Outline each blood parasite and name the species.
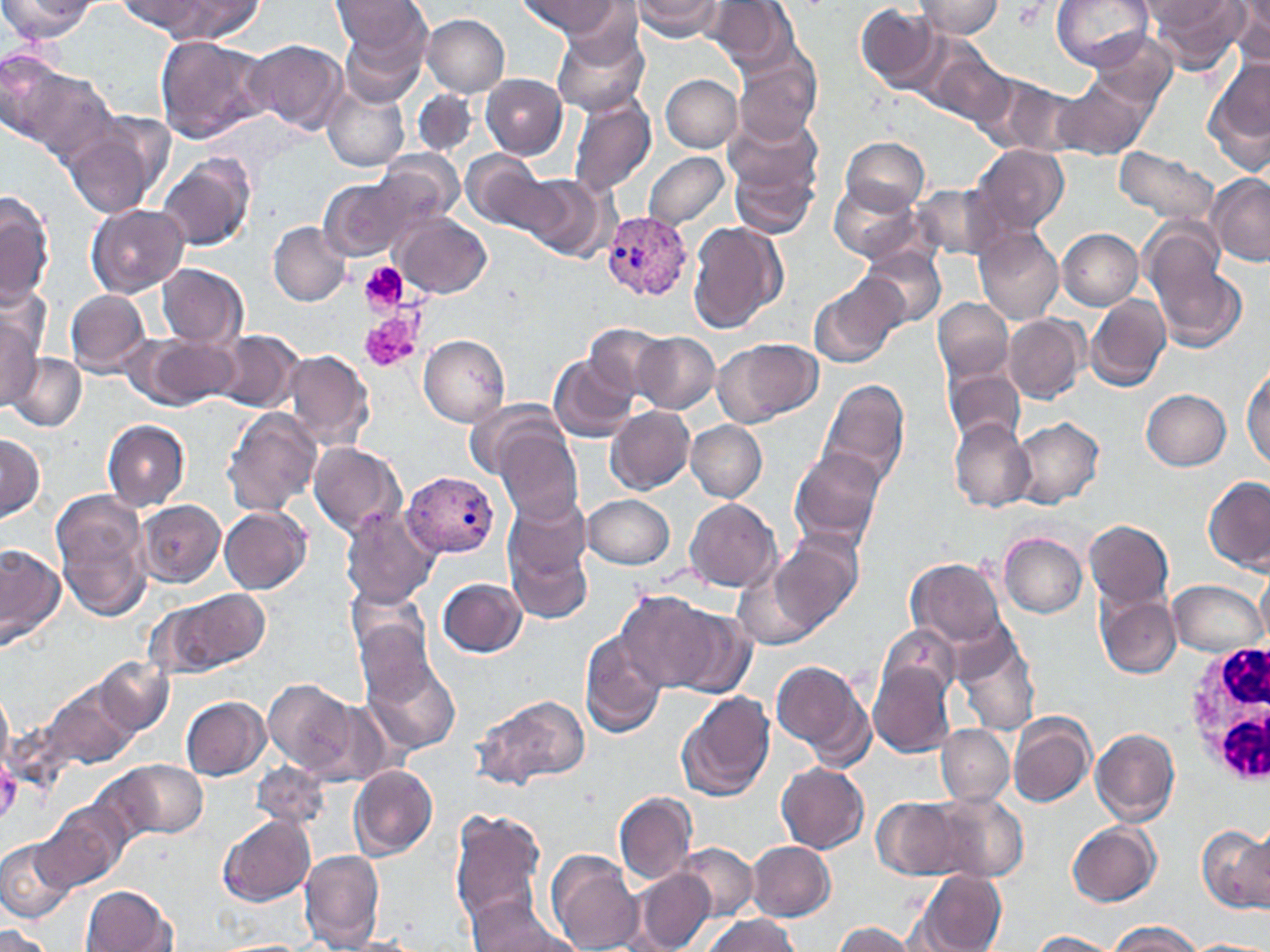
Approximate bounding boxes as named x1/y1/x2/y2 corners in pixels.
Plasmodium vivax-infected red blood cells: (x1=601, y1=212, x2=690, y2=302), (x1=403, y1=472, x2=500, y2=558).
No Plasmodium falciparum, Plasmodium ovale, Plasmodium malariae, Babesia divergens, or Trypanosoma brucei observed.

slide-level diagnosis = Plasmodium vivax
image size = 1270×952 pixels
field of view = single
platelet locations = approximate bounding boxes as named x1/y1/x2/y2 corners in pixels: (x1=1011, y1=2, x2=1047, y2=31), (x1=359, y1=262, x2=410, y2=312), (x1=359, y1=312, x2=419, y2=373)
white blood cell locations = approximate bounding boxes as named x1/y1/x2/y2 corners in pixels: (x1=1183, y1=639, x2=1270, y2=789)
modality = light microscopy
stain = May-Grünwald-Giemsa
magnification = 1000x
preparation = thin blood smear
uninfected red blood cell locations = approximate bounding boxes as named x1/y1/x2/y2 corners in pixels: (x1=0, y1=0, x2=95, y2=41), (x1=121, y1=0, x2=207, y2=34), (x1=155, y1=0, x2=263, y2=43), (x1=333, y1=0, x2=431, y2=72), (x1=520, y1=0, x2=619, y2=38), (x1=633, y1=0, x2=726, y2=41), (x1=1051, y1=0, x2=1154, y2=70), (x1=1141, y1=0, x2=1234, y2=27), (x1=1150, y1=0, x2=1247, y2=70), (x1=705, y1=1, x2=797, y2=72), (x1=915, y1=1, x2=1003, y2=39), (x1=1228, y1=2, x2=1270, y2=67), (x1=855, y1=3, x2=943, y2=94), (x1=422, y1=14, x2=510, y2=96), (x1=551, y1=24, x2=649, y2=118), (x1=338, y1=29, x2=428, y2=108), (x1=1089, y1=31, x2=1178, y2=116), (x1=153, y1=34, x2=269, y2=144), (x1=244, y1=39, x2=347, y2=135), (x1=921, y1=41, x2=1016, y2=129), (x1=0, y1=47, x2=65, y2=143), (x1=732, y1=47, x2=822, y2=147), (x1=1205, y1=55, x2=1270, y2=173), (x1=8, y1=63, x2=115, y2=166), (x1=481, y1=74, x2=567, y2=159), (x1=661, y1=74, x2=742, y2=153), (x1=979, y1=74, x2=1084, y2=156), (x1=1053, y1=79, x2=1149, y2=160), (x1=321, y1=82, x2=409, y2=172), (x1=412, y1=89, x2=476, y2=155), (x1=566, y1=93, x2=657, y2=198), (x1=721, y1=111, x2=822, y2=216), (x1=62, y1=116, x2=169, y2=220), (x1=840, y1=136, x2=931, y2=213), (x1=971, y1=145, x2=1070, y2=232), (x1=1113, y1=146, x2=1224, y2=235), (x1=463, y1=150, x2=557, y2=236), (x1=375, y1=151, x2=463, y2=230), (x1=643, y1=151, x2=731, y2=230), (x1=157, y1=152, x2=256, y2=252), (x1=1207, y1=174, x2=1270, y2=266), (x1=319, y1=176, x2=412, y2=260), (x1=523, y1=176, x2=611, y2=262), (x1=829, y1=181, x2=924, y2=264), (x1=910, y1=182, x2=1011, y2=263), (x1=0, y1=194, x2=53, y2=308), (x1=86, y1=203, x2=188, y2=297), (x1=393, y1=214, x2=493, y2=297), (x1=687, y1=220, x2=788, y2=335), (x1=268, y1=221, x2=351, y2=306), (x1=974, y1=228, x2=1065, y2=324), (x1=1058, y1=228, x2=1144, y2=309), (x1=1148, y1=242, x2=1249, y2=350), (x1=859, y1=246, x2=946, y2=328), (x1=157, y1=264, x2=247, y2=348), (x1=811, y1=273, x2=906, y2=368), (x1=65, y1=289, x2=150, y2=375), (x1=1087, y1=293, x2=1171, y2=391), (x1=933, y1=298, x2=1013, y2=382), (x1=0, y1=312, x2=40, y2=411), (x1=1005, y1=314, x2=1087, y2=403), (x1=584, y1=323, x2=670, y2=399), (x1=214, y1=329, x2=302, y2=412), (x1=633, y1=331, x2=719, y2=414), (x1=418, y1=334, x2=511, y2=426), (x1=142, y1=336, x2=238, y2=407), (x1=714, y1=337, x2=823, y2=426), (x1=282, y1=349, x2=375, y2=452), (x1=7, y1=352, x2=86, y2=431), (x1=549, y1=354, x2=639, y2=442), (x1=1243, y1=360, x2=1270, y2=472), (x1=945, y1=366, x2=1026, y2=447), (x1=819, y1=379, x2=911, y2=493), (x1=1141, y1=389, x2=1231, y2=470), (x1=465, y1=396, x2=563, y2=478), (x1=607, y1=406, x2=694, y2=494), (x1=222, y1=408, x2=322, y2=516), (x1=1011, y1=417, x2=1104, y2=509), (x1=103, y1=419, x2=191, y2=511), (x1=948, y1=419, x2=1036, y2=513), (x1=686, y1=421, x2=766, y2=501), (x1=496, y1=427, x2=584, y2=525), (x1=0, y1=433, x2=44, y2=522), (x1=307, y1=441, x2=406, y2=538), (x1=788, y1=447, x2=887, y2=551), (x1=1205, y1=476, x2=1270, y2=572), (x1=52, y1=490, x2=154, y2=621), (x1=583, y1=493, x2=676, y2=571), (x1=504, y1=494, x2=596, y2=619), (x1=683, y1=497, x2=782, y2=593), (x1=138, y1=500, x2=226, y2=587), (x1=219, y1=505, x2=312, y2=594), (x1=340, y1=507, x2=440, y2=608), (x1=1085, y1=519, x2=1174, y2=610), (x1=999, y1=532, x2=1087, y2=617), (x1=769, y1=535, x2=864, y2=636), (x1=0, y1=543, x2=64, y2=650), (x1=907, y1=557, x2=1007, y2=648), (x1=735, y1=558, x2=823, y2=653), (x1=1254, y1=569, x2=1270, y2=652), (x1=437, y1=576, x2=528, y2=658), (x1=1168, y1=579, x2=1264, y2=657), (x1=346, y1=580, x2=433, y2=666), (x1=159, y1=589, x2=270, y2=677), (x1=614, y1=589, x2=729, y2=691), (x1=1097, y1=592, x2=1181, y2=678), (x1=660, y1=601, x2=758, y2=698), (x1=352, y1=611, x2=449, y2=714), (x1=880, y1=624, x2=961, y2=702), (x1=580, y1=629, x2=668, y2=738), (x1=950, y1=630, x2=1041, y2=734), (x1=362, y1=654, x2=463, y2=755), (x1=92, y1=655, x2=173, y2=739), (x1=772, y1=659, x2=872, y2=764), (x1=871, y1=662, x2=957, y2=755), (x1=32, y1=674, x2=144, y2=780), (x1=263, y1=679, x2=356, y2=776), (x1=0, y1=689, x2=13, y2=775), (x1=677, y1=689, x2=776, y2=802), (x1=470, y1=692, x2=591, y2=790), (x1=180, y1=695, x2=271, y2=780), (x1=1009, y1=713, x2=1097, y2=807), (x1=937, y1=725, x2=1014, y2=805), (x1=1091, y1=727, x2=1181, y2=823), (x1=96, y1=757, x2=209, y2=846), (x1=251, y1=760, x2=328, y2=833), (x1=776, y1=762, x2=869, y2=853), (x1=349, y1=765, x2=438, y2=858), (x1=614, y1=791, x2=698, y2=884), (x1=932, y1=792, x2=1030, y2=881), (x1=870, y1=795, x2=976, y2=881), (x1=33, y1=801, x2=127, y2=895), (x1=450, y1=807, x2=547, y2=929), (x1=216, y1=813, x2=315, y2=906), (x1=1066, y1=822, x2=1162, y2=906), (x1=1197, y1=824, x2=1270, y2=913), (x1=1, y1=839, x2=73, y2=924), (x1=747, y1=840, x2=835, y2=921), (x1=675, y1=844, x2=757, y2=920), (x1=299, y1=849, x2=386, y2=949), (x1=546, y1=849, x2=643, y2=951), (x1=633, y1=868, x2=714, y2=951), (x1=913, y1=870, x2=1007, y2=952), (x1=79, y1=885, x2=178, y2=952), (x1=465, y1=896, x2=580, y2=952), (x1=701, y1=914, x2=802, y2=952), (x1=831, y1=920, x2=923, y2=952), (x1=1107, y1=921, x2=1202, y2=951), (x1=1, y1=926, x2=54, y2=952), (x1=1026, y1=930, x2=1123, y2=951), (x1=208, y1=938, x2=321, y2=952)